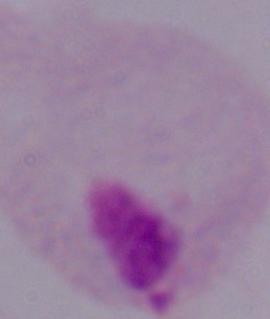

magnification = 1000x
modality = photomicrograph
identification = trichomonad